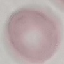

Summary:
  - Malaria status: uninfected
  - Stain: Giemsa
  - Preparation: thin blood smear
  - Capture: smartphone camera at the microscope eyepiece
  - Image type: automatically extracted cell patch, resized to 64 × 64 pixels